Identify the parasite.
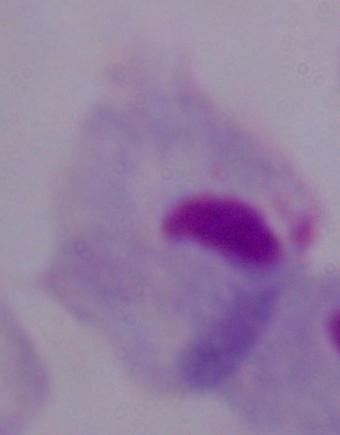

This is a trichomonad.

Photomicrograph. 1000x magnification.